Assess this cell for malaria.
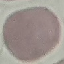

It is uninfected.

Summary:
  - Stain: Giemsa
  - Image type: automatically extracted cell patch, resized to 64 × 64 pixels
  - Preparation: thin smear
  - Capture: smartphone through the microscope eyepiece